Locate every blood parasite and identify its species.
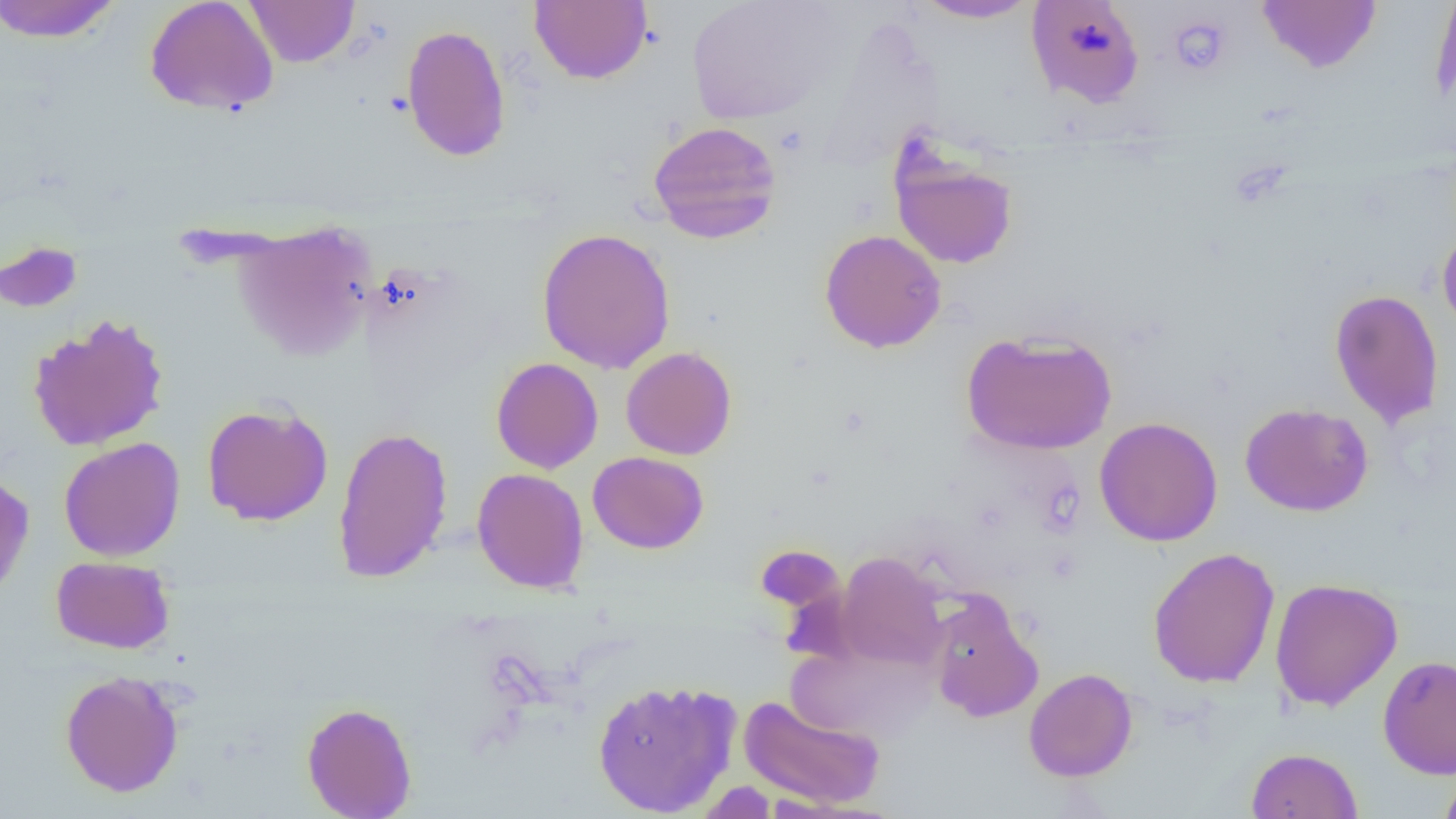
No blood parasites seen.

Summary:
  - Coordinate format: approximate bounding boxes as (x1,y1)-(x2,y2) corner pairs in pixels
  - Uninfected red blood cell locations: (0,0)-(123,43), (144,0)-(280,116), (244,0)-(359,67), (530,0)-(652,85), (685,0)-(843,125), (911,0)-(1041,23), (1026,0)-(1145,108), (1257,0)-(1381,74), (1430,0)-(1456,109), (401,24)-(512,162), (647,120)-(782,244), (888,144)-(1019,269), (233,220)-(376,361), (1437,226)-(1456,338), (536,227)-(676,375), (819,229)-(947,353), (0,240)-(83,313), (1329,288)-(1444,429), (27,313)-(170,452), (961,329)-(1117,456), (621,346)-(737,460), (491,357)-(603,474), (1240,402)-(1373,517), (202,403)-(333,526), (1095,416)-(1223,547), (332,425)-(453,584), (58,436)-(185,562), (588,451)-(709,554), (471,467)-(589,594), (0,472)-(35,603), (1148,546)-(1280,688), (835,552)-(947,671), (51,555)-(175,654), (1269,577)-(1403,712), (925,591)-(1043,723), (789,638)-(936,744), (1377,655)-(1456,779), (1024,667)-(1138,782), (60,670)-(184,797), (592,678)-(742,817), (738,694)-(886,810), (302,701)-(417,819), (1246,747)-(1362,818), (1438,769)-(1456,819), (695,781)-(777,819)
  - Platelet locations: (1167,14)-(1232,77), (774,125)-(809,157)
  - Slide-level diagnosis: negative for blood parasites
  - Preparation: thin blood film
  - Magnification: 1000x
  - Image size: 1456×819 pixels
  - Field of view: single
  - Modality: light microscopy